Name the parasite shown.
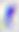

Toxoplasma gondii.

modality = micrograph
magnification = 400x